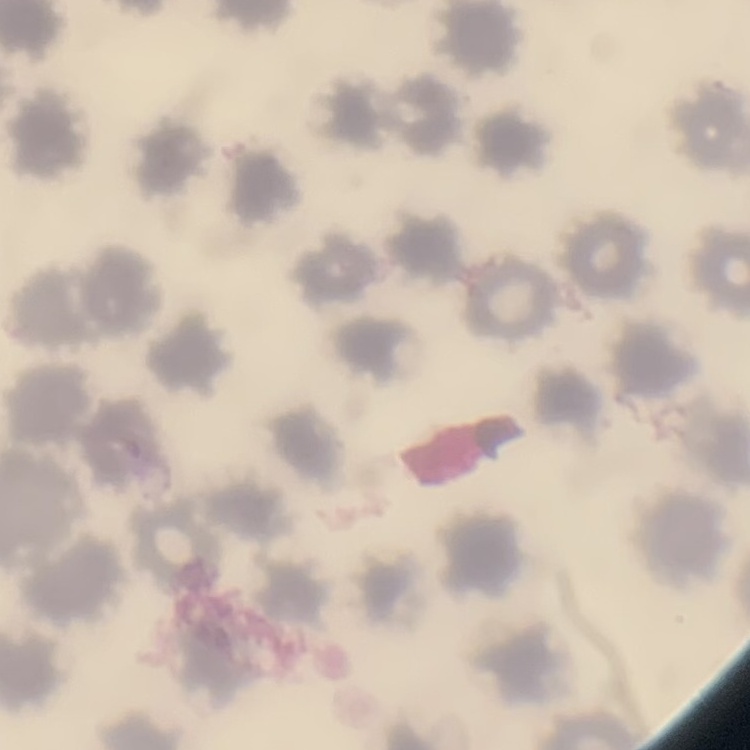
Summary:
  - Red blood cell morphology: no rouleaux formation
  - Preparation: thin blood smear
  - Stain: Field's or Giemsa
  - Image type: square crop of a larger photomicrograph